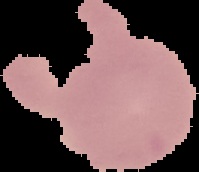
image type = cell region segmented out of the field of view; surrounding area masked to black
result = no malaria parasites seen
preparation = thin blood film
image size = 199×172 pixels